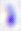
Toxoplasma gondii is seen. Micrograph. Captured at 400x magnification.